Assess this cell for malaria.
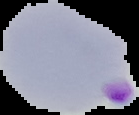
Parasitized.

The area outside the segmented cell region is set to black. Image is 139×115 pixels. From a thin blood smear.